Assess the morphology of the erythrocytes.
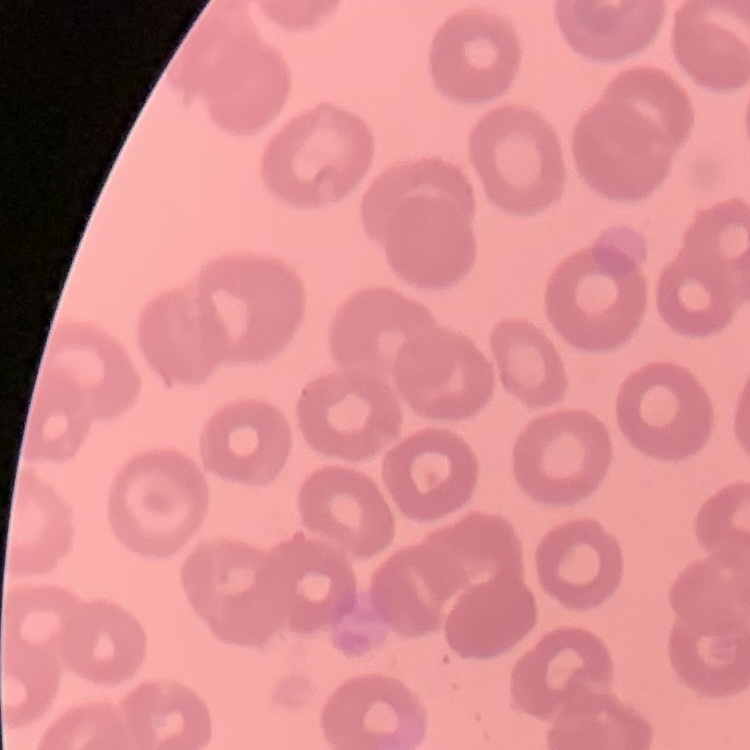

No rouleaux formation.

Stained with either Field's or Giemsa. Thin blood film. One tile cut from a larger photomicrograph.